State which parasite is depicted.
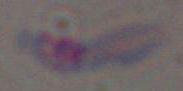

This is Toxoplasma gondii.

Micrograph. 1000x magnification.